Assess this cell for malaria.
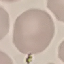
It is uninfected.

Cell patch, automatically extracted from a larger field of view and resized to 64 × 64 pixels. Giemsa stain. Thin smear of blood. Photographed with a smartphone camera at the microscope eyepiece.